Give the extent of all Plasmodium ovale-infected red blood cells.
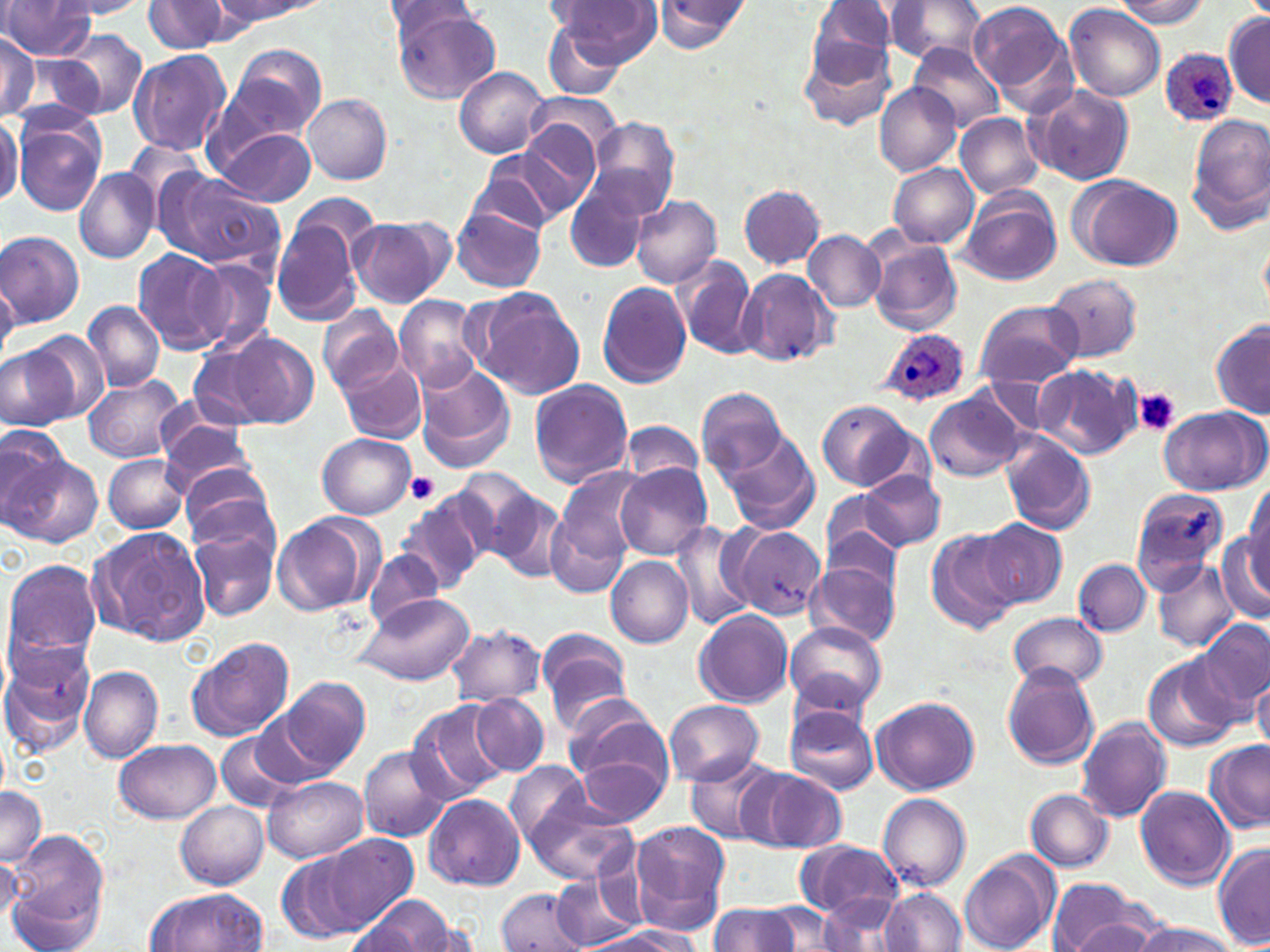
Approximate bounding boxes as (x1,y1)-(x2,y2) corner pairs in pixels.
Plasmodium ovale-infected red blood cells: (1160,49)-(1238,126), (879,328)-(970,408).

Summary:
  - Uninfected red blood cell locations: (546,0)-(657,77), (968,0)-(1076,108), (0,1)-(99,59), (55,1)-(154,19), (143,1)-(233,54), (214,1)-(312,25), (378,1)-(482,43), (808,1)-(897,75), (881,1)-(988,66), (1113,1)-(1210,30), (651,2)-(748,51), (1064,3)-(1165,103), (390,7)-(501,104), (1224,10)-(1270,107), (541,19)-(628,100), (56,29)-(147,119), (0,32)-(40,122), (797,35)-(897,132), (909,43)-(1005,135), (229,45)-(327,141), (128,50)-(231,157), (454,66)-(549,158), (875,83)-(960,177), (1027,84)-(1135,186), (304,93)-(392,184), (520,100)-(616,197), (0,112)-(22,209), (955,113)-(1043,198), (1186,113)-(1270,231), (13,114)-(105,215), (587,118)-(682,217), (214,127)-(317,207), (504,127)-(599,220), (124,140)-(207,214), (475,148)-(576,233), (887,164)-(979,248), (73,167)-(159,262), (156,170)-(282,274), (1070,174)-(1183,271), (564,179)-(650,274), (738,184)-(826,270), (960,187)-(1062,286), (293,190)-(381,261), (630,195)-(722,289), (452,206)-(547,294), (272,213)-(365,325), (350,217)-(451,307), (0,229)-(85,326), (804,230)-(886,312), (866,236)-(963,336), (133,248)-(229,354), (674,254)-(758,360), (190,258)-(277,354), (735,267)-(837,368), (1045,274)-(1143,362), (0,276)-(23,355), (597,282)-(691,387), (471,291)-(585,398), (394,295)-(484,393), (82,300)-(165,392), (975,300)-(1082,389), (316,305)-(403,395), (1212,322)-(1270,418), (26,330)-(111,420), (224,331)-(319,428), (184,338)-(290,433), (1,345)-(77,429), (338,356)-(427,444), (414,363)-(515,472), (1032,365)-(1141,460), (83,375)-(185,464), (529,378)-(635,488), (696,386)-(787,477), (924,389)-(1026,481), (818,400)-(916,492), (1159,406)-(1268,497), (155,414)-(256,494), (619,420)-(706,487), (0,425)-(69,522), (716,430)-(820,534), (318,433)-(415,519), (1001,433)-(1097,535), (6,454)-(102,547), (104,454)-(189,533), (176,461)-(278,553), (616,465)-(712,560), (555,466)-(649,565), (453,469)-(541,558), (859,471)-(946,550), (1245,481)-(1270,577), (1130,486)-(1228,589), (490,488)-(569,581), (820,490)-(902,568), (401,492)-(491,590), (544,505)-(632,598), (272,513)-(375,616), (977,518)-(1066,608), (669,519)-(757,631), (90,526)-(211,646), (188,526)-(277,623), (729,526)-(827,620), (823,526)-(902,597), (926,527)-(1022,635), (1217,530)-(1270,622), (363,549)-(446,630), (606,557)-(693,648), (1074,558)-(1152,637), (3,559)-(102,668), (808,560)-(900,648), (1152,560)-(1238,652), (353,592)-(475,687), (693,609)-(793,708), (1008,611)-(1108,690), (1194,617)-(1270,714), (785,621)-(886,714), (447,625)-(546,707), (536,629)-(632,728), (186,636)-(294,742), (0,638)-(96,757), (1141,653)-(1241,753), (78,664)-(163,763), (1002,664)-(1101,769), (1252,673)-(1270,751), (280,675)-(371,774), (469,693)-(549,777), (872,695)-(981,795), (562,696)-(671,793), (406,700)-(510,803), (664,700)-(764,785), (785,705)-(879,796), (253,710)-(345,788), (1075,718)-(1171,822), (215,731)-(298,812), (113,740)-(224,824), (1203,740)-(1268,831), (358,746)-(448,843), (572,754)-(671,828), (686,756)-(781,843), (505,759)-(591,848), (750,768)-(847,852), (263,776)-(367,863), (1135,785)-(1235,889), (0,787)-(46,870), (1025,789)-(1114,871), (520,792)-(638,886), (424,793)-(526,891), (879,793)-(971,892), (176,801)-(267,890), (628,821)-(731,935), (6,830)-(108,944), (313,833)-(420,932), (793,838)-(902,919), (1213,844)-(1269,950), (959,850)-(1055,952), (276,852)-(366,943), (0,854)-(20,924), (552,873)-(640,951), (1047,878)-(1151,952), (144,887)-(267,952), (495,887)-(590,950), (883,888)-(967,952), (820,893)-(907,952), (359,895)-(457,950), (708,901)-(801,952), (759,902)-(844,950), (1063,915)-(1162,952), (1132,920)-(1239,952), (585,927)-(699,952)
  - Platelet locations: (1132,387)-(1181,436), (406,470)-(441,504)
  - Slide-level diagnosis: Plasmodium ovale
  - Modality: optical microscopy
  - Field of view: single
  - Stain: May-Grünwald-Giemsa
  - Preparation: thin blood film
  - Image size: 1270×952 pixels
  - Magnification: 1000x